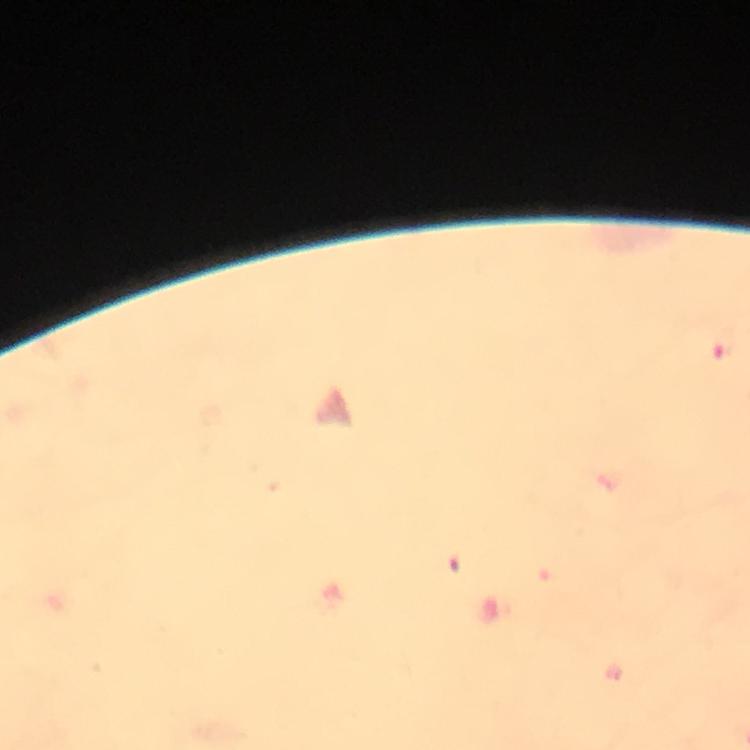
Approximate centers as [x, y] in pixels. Malaria parasite locations: [724, 346]. Photographed with a smartphone mounted on the microscope. 100x magnification. Immersion oil applied. Image is 750×750 pixels. Giemsa-stained preparation. Thick smear. From a diagnostic examination for malaria. A crop from one field of view.